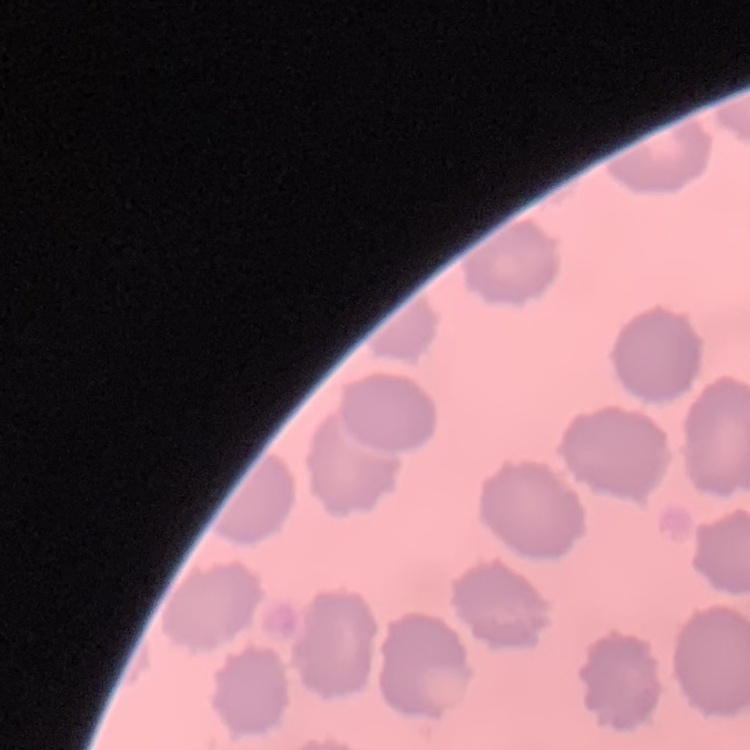

The erythrocytes show no rouleaux formation. Thin peripheral smear. Field's or Giemsa stain. Square crop of a larger photomicrograph.